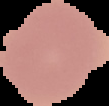
result = no malaria parasites seen
image type = segmented cell region on a black background
image size = 109×106 pixels
preparation = thin blood film